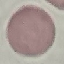
malaria status = uninfected
capture = smartphone through the microscope eyepiece
preparation = thin blood film
image type = cell patch, automatically extracted from a larger field of view and resized to 64 × 64 pixels
stain = Giemsa